Outline each Plasmodium vivax-infected red blood cell.
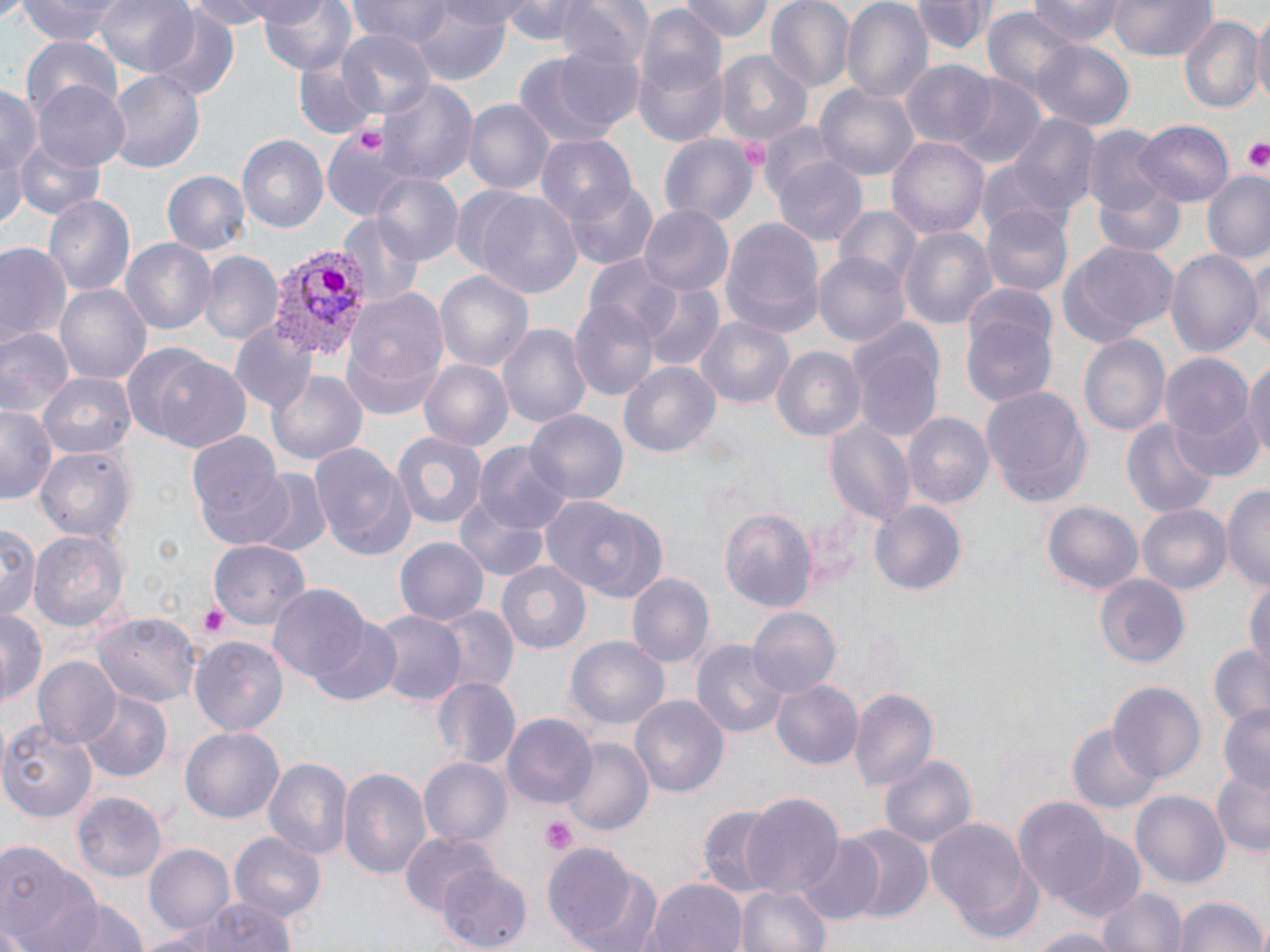
Approximate bounding boxes as (x1,y1)-(x2,y2) corner pairs in pixels.
Plasmodium vivax-infected red blood cells: (268,243)-(367,360).

Uninfected red blood cell locations: (15,0)-(128,44), (94,0)-(200,79), (187,0)-(298,32), (257,0)-(359,77), (348,0)-(453,47), (501,0)-(601,47), (556,0)-(655,72), (677,0)-(775,42), (766,0)-(855,91), (839,0)-(933,107), (1025,0)-(1130,46), (1109,0)-(1216,62), (910,1)-(994,57), (410,2)-(514,86), (977,7)-(1083,110), (150,11)-(240,102), (1250,12)-(1270,111), (1177,16)-(1260,111), (631,17)-(728,143), (333,27)-(435,121), (23,33)-(122,120), (1034,40)-(1133,132), (515,47)-(639,150), (714,48)-(812,147), (294,52)-(382,139), (900,61)-(997,151), (106,69)-(205,175), (946,75)-(1045,168), (380,80)-(477,187), (814,82)-(919,184), (3,83)-(41,196), (37,86)-(128,169), (463,100)-(554,197), (1007,115)-(1101,222), (1136,118)-(1234,204), (318,125)-(413,226), (1084,126)-(1175,224), (659,133)-(758,227), (235,135)-(329,235), (535,136)-(637,228), (888,137)-(990,237), (11,138)-(104,220), (772,157)-(869,249), (976,157)-(1073,243), (161,170)-(250,258), (371,172)-(462,268), (1203,173)-(1270,264), (1092,177)-(1188,258), (563,179)-(658,269), (456,185)-(584,298), (42,193)-(135,300), (640,205)-(732,297), (980,205)-(1072,298), (835,208)-(924,291), (340,212)-(425,304), (719,216)-(825,338), (897,225)-(996,331), (120,237)-(215,335), (1057,240)-(1179,347), (1164,244)-(1259,357), (2,245)-(71,350), (201,252)-(283,344), (813,252)-(908,346), (1247,253)-(1269,360), (582,255)-(692,350), (434,270)-(534,372), (54,280)-(150,384), (640,283)-(723,371), (341,288)-(449,416), (962,295)-(1058,413), (569,298)-(661,402), (849,317)-(945,442), (698,318)-(793,407), (231,321)-(316,410), (499,322)-(591,433), (0,324)-(74,418), (1080,334)-(1171,439), (126,346)-(252,454), (772,346)-(865,444), (1161,350)-(1259,468), (1244,355)-(1270,467), (420,360)-(513,452), (620,361)-(721,458), (271,370)-(366,467), (39,371)-(135,460), (981,386)-(1093,508), (1,406)-(57,504), (899,408)-(993,509), (527,410)-(627,507), (824,418)-(914,525), (1121,419)-(1218,520), (388,431)-(489,528), (186,433)-(291,545), (310,442)-(416,560), (475,442)-(570,536), (35,444)-(135,543), (252,470)-(332,558), (1222,484)-(1270,593), (454,492)-(551,581), (545,495)-(662,601), (868,499)-(968,598), (1042,500)-(1144,599), (1137,504)-(1231,596), (719,506)-(818,613), (0,522)-(41,625), (28,529)-(130,631), (395,537)-(490,626), (207,540)-(312,626), (496,559)-(593,654), (627,572)-(713,669), (1095,574)-(1189,668), (1244,574)-(1270,672), (267,585)-(378,690), (434,603)-(518,695), (748,607)-(841,697), (0,609)-(45,706), (373,611)-(464,706), (94,613)-(202,705), (306,617)-(403,707), (191,636)-(289,738), (565,636)-(669,732), (692,638)-(790,741), (1207,645)-(1270,727), (33,657)-(122,751), (431,676)-(523,767), (770,679)-(862,771), (1107,681)-(1204,780), (849,686)-(938,795), (78,690)-(173,782), (631,695)-(729,798), (1216,703)-(1270,794), (502,713)-(595,809), (0,718)-(97,822), (1068,723)-(1164,816), (180,727)-(283,825), (562,737)-(652,837), (879,754)-(976,853), (265,757)-(353,862), (420,757)-(513,849), (340,766)-(431,881), (1211,771)-(1270,856), (1133,791)-(1229,889), (73,793)-(167,884), (739,796)-(844,902), (1013,800)-(1113,901), (696,803)-(790,896), (926,815)-(1040,937), (834,824)-(933,923), (400,831)-(497,915), (229,833)-(327,923), (1055,834)-(1148,925), (796,836)-(886,924), (546,841)-(644,950), (0,843)-(103,952), (144,843)-(234,935), (436,867)-(532,949), (576,867)-(666,952), (645,876)-(747,952), (735,883)-(831,952), (1096,887)-(1186,952), (1171,895)-(1267,952), (56,897)-(150,952), (146,900)-(295,952), (1017,926)-(1129,951). Platelet locations: (359,128)-(387,154), (1241,136)-(1270,176), (744,140)-(771,169), (195,603)-(233,638), (542,816)-(578,854). Slide-level diagnosis: Plasmodium vivax. Image is 1270×952 pixels. Thin blood film. 1000x magnification. Light microscopy. Single field of view. May-Grünwald-Giemsa stain.